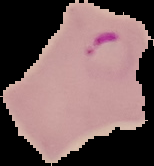

From a thin blood film. Image is 154×166 pixels. Result: malaria parasites identified. The area outside the segmented cell region is set to black.